Classify this cell by malaria status.
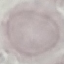

It is uninfected.

Photographed with a smartphone camera at the microscope eyepiece. Automatically extracted cell patch, resized to 64 × 64 pixels. Thin blood smear. Giemsa stain.